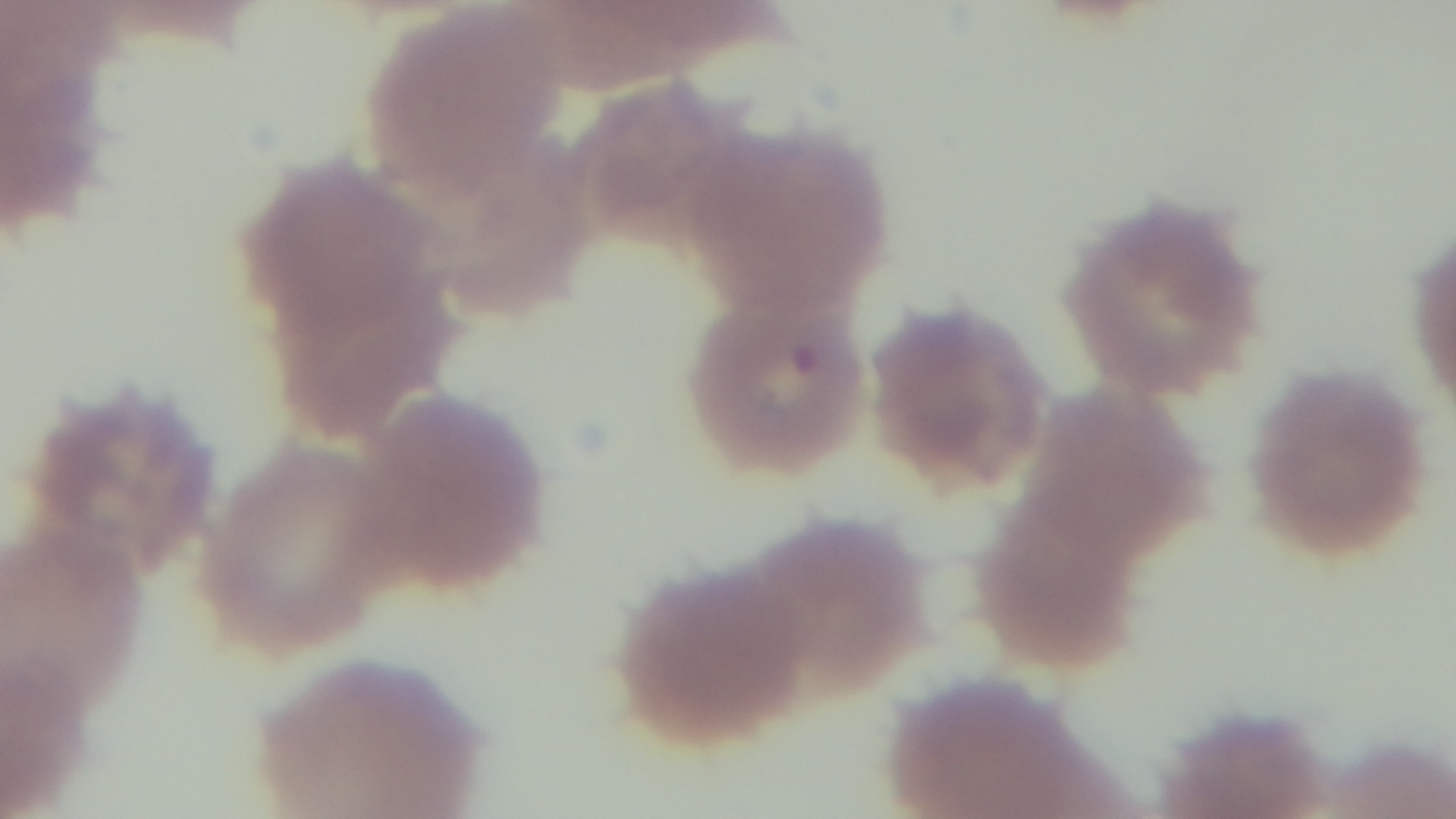

{
  "modality": "light microscopy",
  "capture": "mounted 4K digital camera",
  "malaria_status": "infected",
  "objective": "100x oil immersion",
  "preparation": "thin smear",
  "stain": "Giemsa",
  "field_of_view": "one from the slide"
}